Identify the parasite.
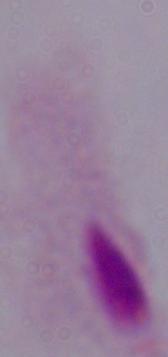

A trichomonad.

magnification: 1000x
modality: photomicrograph